Locate every Plasmodium parasite.
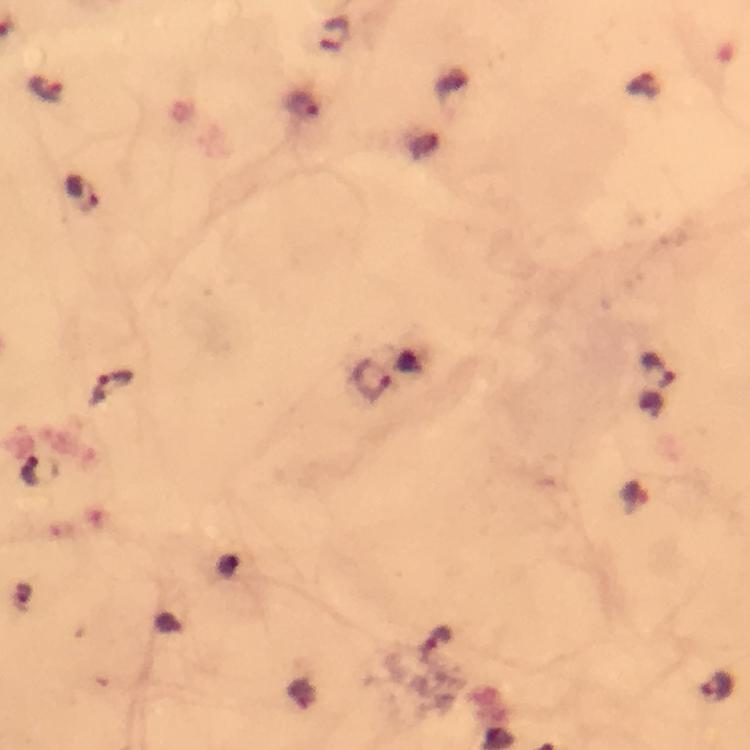

Approximate centers as {x, y} in pixels.
Plasmodium parasites: {335, 33}, {644, 85}, {47, 91}, {303, 106}, {82, 193}, {656, 369}, {370, 380}, {110, 386}, {41, 471}, {438, 639}, {719, 687}.

capture = smartphone photograph through a microscope
context = from a diagnostic examination for malaria
preparation = thick smear
stain = Giemsa
magnification = 100x
immersion oil = used
image size = 750×750 pixels
cropped from = one field of view